Identify the parasite.
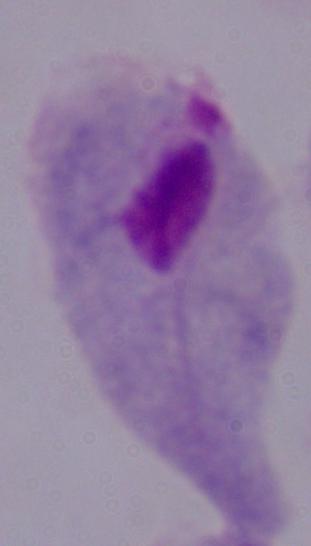

This is a trichomonad.

Micrograph. Captured at 1000x magnification.